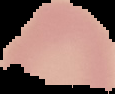
Summary:
  - Image type: cell region segmented out of the field of view; surrounding area masked to black
  - Preparation: thin blood smear
  - Result: no malaria parasites seen
  - Image size: 115×94 pixels